Classify this cell by malaria status.
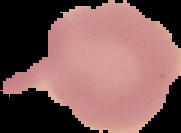
Uninfected.

Image is 181×133 pixels. Cell region segmented out of the field of view; the surrounding area is masked to black. From a thin blood smear.